Give the position of every malaria parasite.
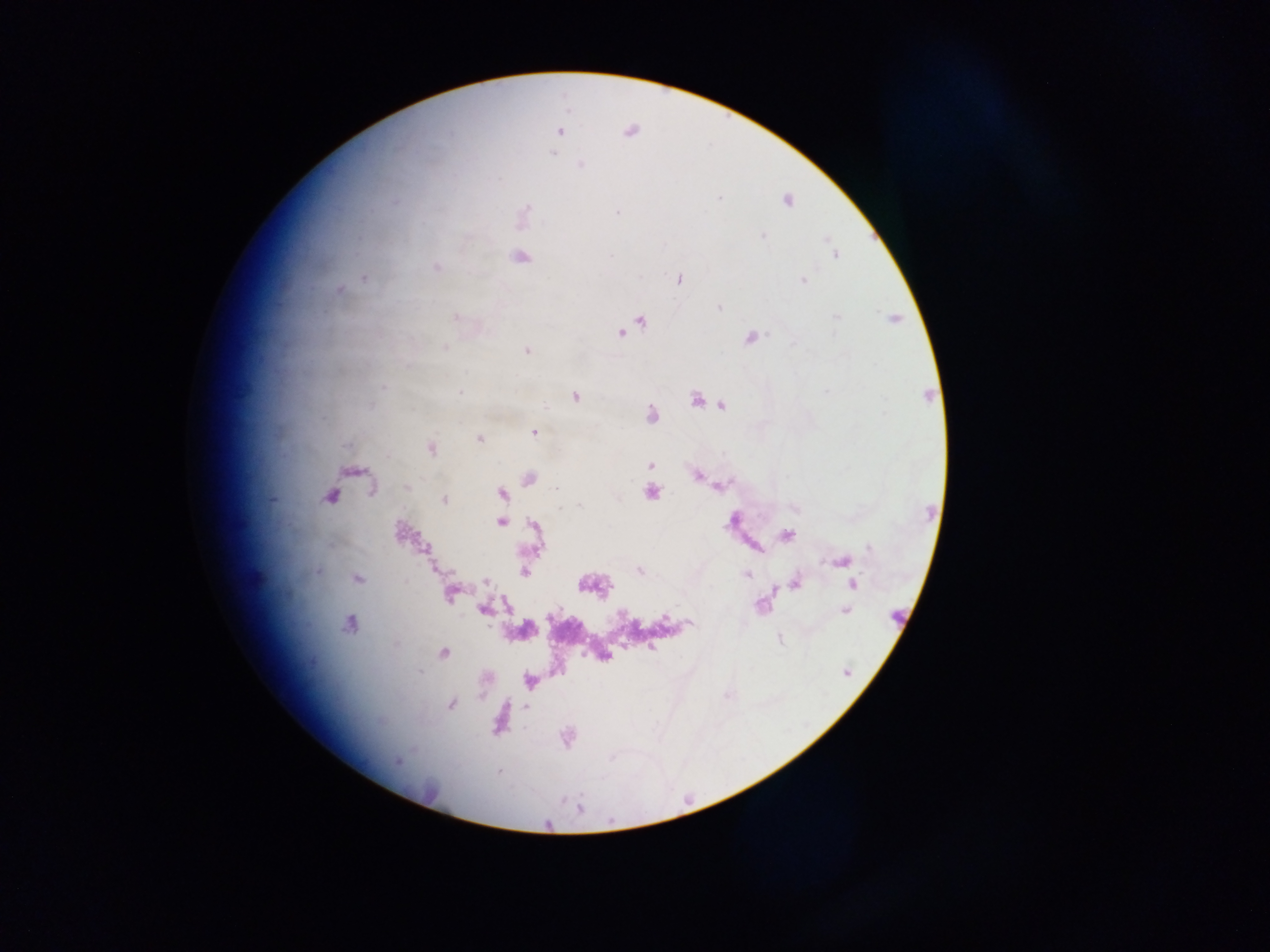

Approximate centers as (x, y) in pixels.
Malaria parasites: (560, 131), (630, 131), (554, 155), (582, 165), (787, 200), (528, 207), (617, 212), (763, 235), (827, 240), (836, 256), (610, 257), (522, 258), (436, 266), (363, 277), (679, 278), (802, 280), (340, 290), (717, 307), (453, 315), (836, 316), (640, 319), (893, 319), (621, 334), (750, 338), (445, 348), (527, 351), (383, 386), (460, 393), (576, 397), (695, 399), (721, 406), (653, 416), (533, 433), (479, 438), (430, 449), (651, 463), (698, 477), (529, 478), (407, 486), (555, 488), (717, 488), (652, 493), (501, 494), (330, 496), (274, 499), (444, 500), (579, 506), (561, 508), (794, 508), (500, 522), (532, 525), (400, 530), (787, 535), (868, 545), (841, 561), (638, 571), (524, 572), (745, 574), (258, 576), (357, 579), (487, 582), (797, 584), (852, 584), (771, 589), (448, 594), (482, 609), (845, 612), (663, 617), (690, 622), (349, 624), (654, 646), (444, 653), (450, 705), (399, 762).

One field of view. Thick blood smear. Mobile-phone photograph taken through the microscope. Sample from Ghana. Image is 1270×952 pixels.